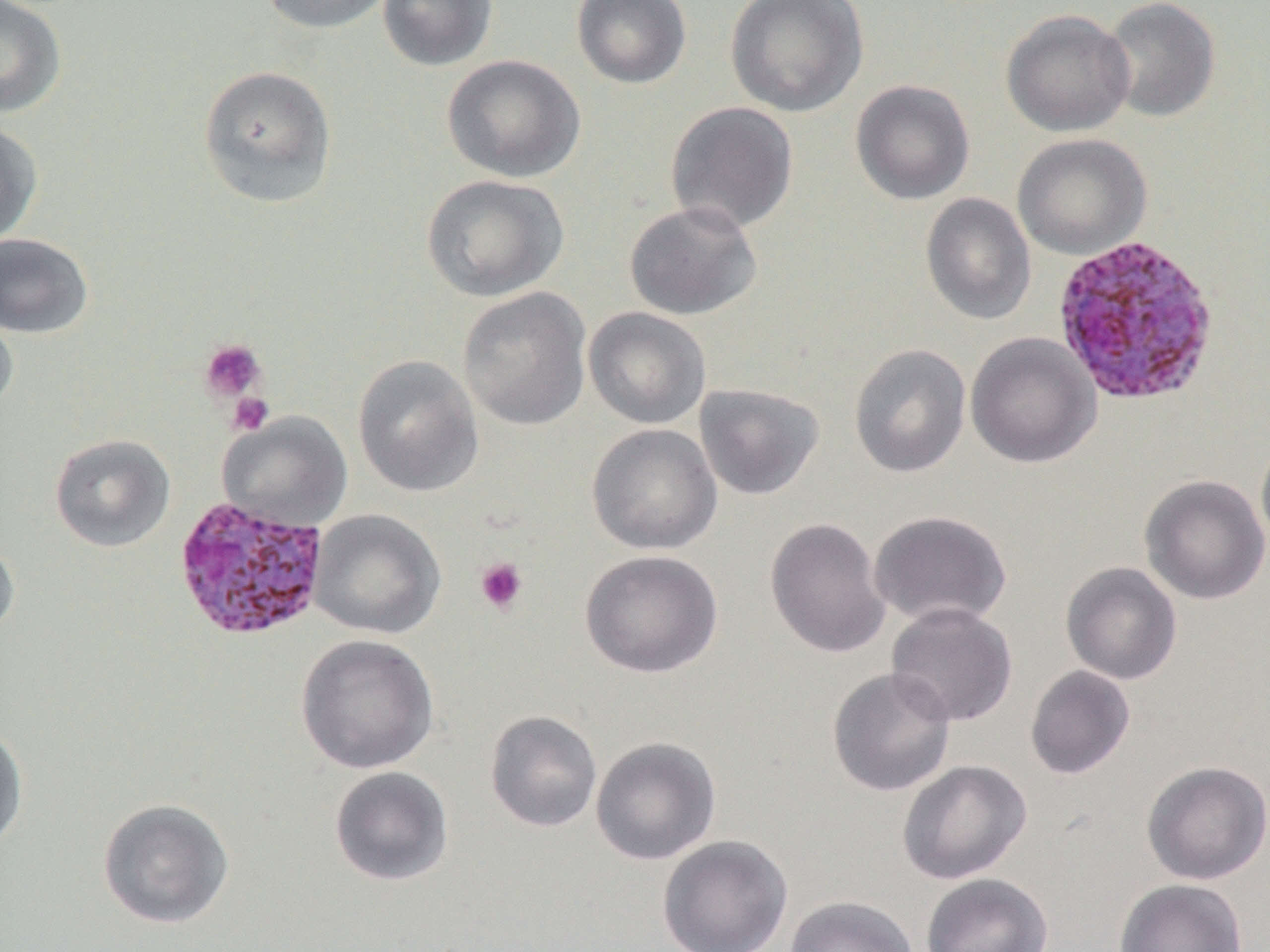

Approximate bounding boxes as (x1, y1, x2, y2) in pixels. Uninfected red blood cell locations: (0, 0, 67, 118), (259, 0, 396, 34), (377, 0, 498, 71), (571, 0, 692, 89), (726, 0, 869, 117), (1100, 0, 1221, 123), (1000, 9, 1135, 137), (441, 54, 586, 183), (197, 64, 338, 209), (850, 80, 975, 205), (665, 101, 799, 234), (0, 120, 44, 248), (1012, 133, 1153, 260), (421, 174, 569, 302), (920, 192, 1036, 326), (623, 200, 763, 320), (0, 233, 94, 339), (456, 286, 593, 432), (0, 301, 19, 418), (583, 306, 712, 429), (965, 331, 1101, 469), (197, 340, 268, 403), (848, 343, 971, 478), (352, 354, 484, 497), (694, 383, 825, 500), (217, 412, 353, 531), (586, 423, 722, 554), (1255, 432, 1270, 554), (49, 433, 175, 552), (1139, 474, 1270, 605), (308, 509, 445, 639), (868, 510, 1013, 629), (764, 517, 891, 659), (0, 534, 20, 642), (579, 549, 724, 678), (1060, 561, 1183, 685), (886, 602, 1018, 727), (295, 634, 439, 774), (1025, 665, 1135, 779), (826, 666, 957, 797), (484, 710, 603, 833), (0, 723, 29, 854), (590, 736, 722, 865), (897, 759, 1032, 885), (1141, 760, 1270, 885), (329, 766, 454, 887), (97, 797, 234, 929), (657, 835, 793, 952), (920, 872, 1054, 952), (1114, 878, 1248, 952), (785, 895, 918, 952). Plasmodium ovale-infected red blood cell locations: (1050, 234, 1222, 408), (176, 493, 332, 641). Platelet locations: (199, 339, 267, 403), (228, 392, 274, 435), (474, 557, 528, 615). Slide-level diagnosis: Plasmodium ovale. One field of a larger specimen. Thin blood smear. 1000x magnification. Optical microscopy. Image is 1270×952 pixels.